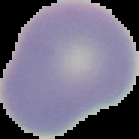

image size = 139×139 pixels
malaria status = uninfected
preparation = thin blood film
image type = cell region segmented out of the field of view; surrounding area masked to black